Classify this cell by malaria status.
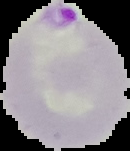

Parasitized.

image size = 130×151 pixels
preparation = thin blood film
image type = cell region segmented out of the field of view; surrounding area masked to black